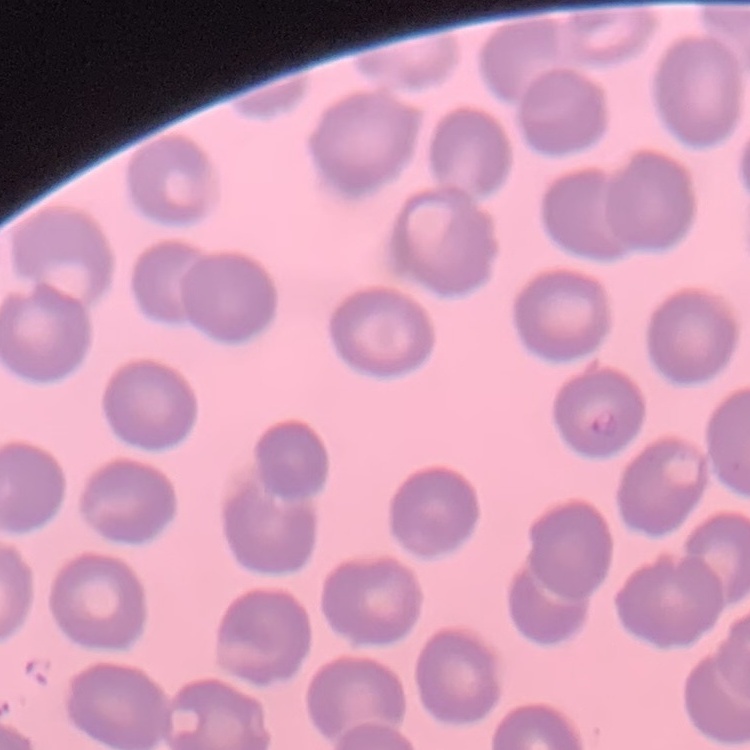 The red blood cells show no rouleaux formation. Field's or Giemsa stain. Square crop of a larger photomicrograph. Thin blood smear.